Describe the morphology of the red blood cells.
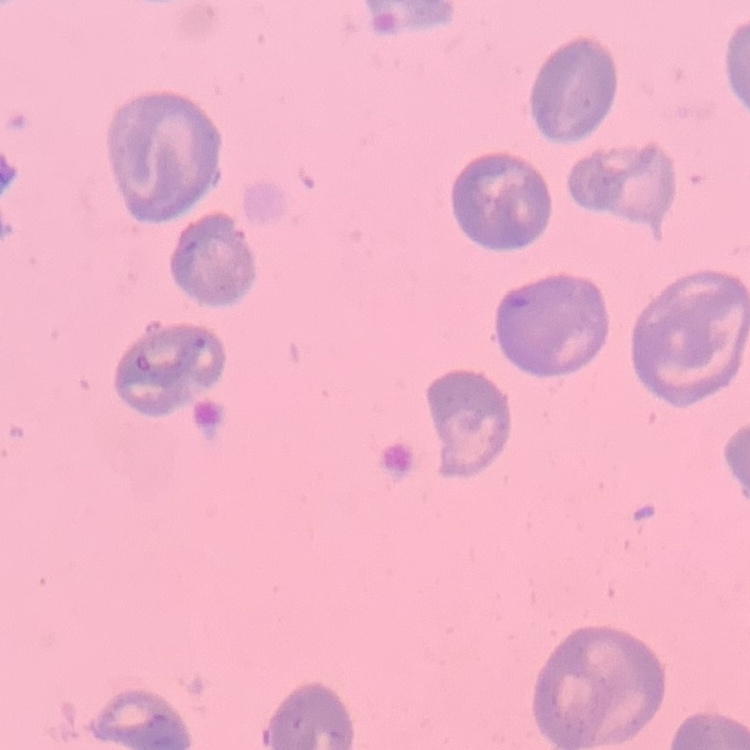
No rouleaux formation.

Summary:
  - Stain: Field's or Giemsa
  - Preparation: thin peripheral smear
  - Image type: square crop of a larger photomicrograph